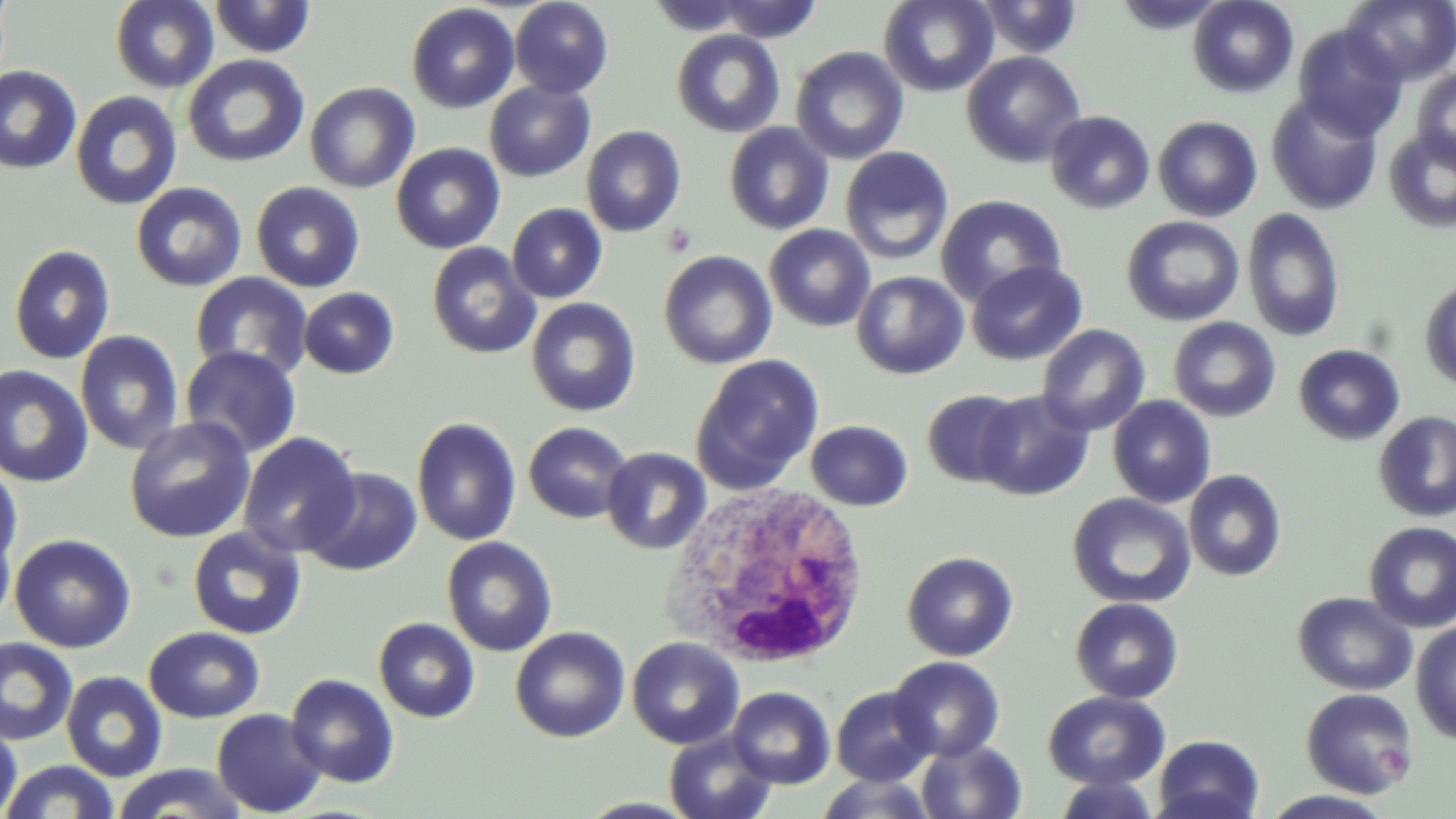

{
  "slide_level_diagnosis": "no evidence of blood parasites",
  "modality": "light microscopy",
  "platelet_locations": "approximate bounding boxes as named x1/y1/x2/y2 corners in pixels: (x1=661, y1=222, x2=699, y2=257)",
  "preparation": "thin blood smear",
  "image_size": "1456×819 pixels",
  "stain": "May-Grünwald-Giemsa",
  "white_blood_cell_locations": "approximate bounding boxes as named x1/y1/x2/y2 corners in pixels: (x1=667, y1=483, x2=873, y2=671)",
  "magnification": "1000x",
  "field_of_view": "one of a larger specimen",
  "uninfected_red_blood_cell_locations": "approximate bounding boxes as named x1/y1/x2/y2 corners in pixels: (x1=110, y1=0, x2=219, y2=93), (x1=208, y1=0, x2=315, y2=59), (x1=714, y1=0, x2=823, y2=43), (x1=878, y1=0, x2=999, y2=97), (x1=974, y1=0, x2=1084, y2=59), (x1=1113, y1=0, x2=1228, y2=34), (x1=1187, y1=0, x2=1299, y2=98), (x1=1342, y1=0, x2=1456, y2=85), (x1=510, y1=1, x2=613, y2=98), (x1=407, y1=3, x2=519, y2=113), (x1=1292, y1=23, x2=1408, y2=141), (x1=671, y1=29, x2=786, y2=138), (x1=790, y1=46, x2=909, y2=164), (x1=961, y1=51, x2=1086, y2=169), (x1=182, y1=54, x2=309, y2=168), (x1=0, y1=65, x2=83, y2=175), (x1=1412, y1=69, x2=1456, y2=170), (x1=484, y1=80, x2=596, y2=182), (x1=305, y1=82, x2=420, y2=193), (x1=70, y1=90, x2=183, y2=210), (x1=1266, y1=93, x2=1384, y2=215), (x1=1045, y1=110, x2=1156, y2=214), (x1=1152, y1=115, x2=1263, y2=222), (x1=724, y1=122, x2=835, y2=235), (x1=581, y1=125, x2=686, y2=237), (x1=1383, y1=128, x2=1456, y2=234), (x1=391, y1=143, x2=505, y2=254), (x1=839, y1=146, x2=955, y2=265), (x1=250, y1=181, x2=366, y2=293), (x1=131, y1=182, x2=248, y2=292), (x1=936, y1=194, x2=1067, y2=307), (x1=506, y1=203, x2=608, y2=303), (x1=1242, y1=208, x2=1345, y2=343), (x1=1121, y1=216, x2=1244, y2=326), (x1=764, y1=224, x2=876, y2=332), (x1=426, y1=242, x2=541, y2=359), (x1=8, y1=244, x2=116, y2=365), (x1=658, y1=250, x2=777, y2=369), (x1=966, y1=260, x2=1088, y2=365), (x1=851, y1=271, x2=969, y2=379), (x1=190, y1=272, x2=313, y2=381), (x1=1419, y1=276, x2=1456, y2=392), (x1=299, y1=287, x2=399, y2=379), (x1=527, y1=297, x2=641, y2=416), (x1=1168, y1=316, x2=1281, y2=422), (x1=1036, y1=324, x2=1151, y2=437), (x1=75, y1=330, x2=184, y2=455), (x1=1293, y1=344, x2=1406, y2=446), (x1=180, y1=346, x2=302, y2=459), (x1=690, y1=353, x2=825, y2=493), (x1=0, y1=365, x2=94, y2=487), (x1=922, y1=388, x2=1025, y2=488), (x1=974, y1=389, x2=1094, y2=501), (x1=1108, y1=395, x2=1216, y2=508), (x1=1373, y1=411, x2=1456, y2=522), (x1=124, y1=416, x2=256, y2=544), (x1=412, y1=417, x2=522, y2=546), (x1=805, y1=419, x2=913, y2=511), (x1=524, y1=421, x2=634, y2=524), (x1=237, y1=431, x2=361, y2=558), (x1=601, y1=446, x2=712, y2=555), (x1=0, y1=463, x2=24, y2=573), (x1=303, y1=467, x2=423, y2=576), (x1=1184, y1=469, x2=1287, y2=581), (x1=1067, y1=492, x2=1196, y2=609), (x1=0, y1=517, x2=17, y2=633), (x1=1363, y1=521, x2=1456, y2=632), (x1=187, y1=526, x2=307, y2=640), (x1=9, y1=533, x2=137, y2=652), (x1=442, y1=536, x2=557, y2=656), (x1=901, y1=551, x2=1019, y2=661), (x1=1292, y1=592, x2=1417, y2=695), (x1=1070, y1=597, x2=1184, y2=704), (x1=373, y1=617, x2=480, y2=723), (x1=1410, y1=621, x2=1456, y2=744), (x1=143, y1=626, x2=265, y2=723), (x1=509, y1=626, x2=630, y2=743), (x1=0, y1=637, x2=78, y2=746), (x1=627, y1=637, x2=745, y2=749), (x1=887, y1=656, x2=1005, y2=762), (x1=61, y1=671, x2=167, y2=782), (x1=285, y1=673, x2=400, y2=788), (x1=831, y1=686, x2=936, y2=786), (x1=727, y1=687, x2=836, y2=789), (x1=1301, y1=688, x2=1418, y2=798), (x1=1043, y1=690, x2=1170, y2=790), (x1=212, y1=708, x2=327, y2=817), (x1=0, y1=721, x2=23, y2=818), (x1=664, y1=729, x2=777, y2=819), (x1=1152, y1=734, x2=1265, y2=819), (x1=916, y1=739, x2=1027, y2=819), (x1=1, y1=760, x2=121, y2=819), (x1=111, y1=763, x2=250, y2=818), (x1=815, y1=773, x2=938, y2=818), (x1=1052, y1=776, x2=1162, y2=818), (x1=1258, y1=790, x2=1398, y2=818)"
}